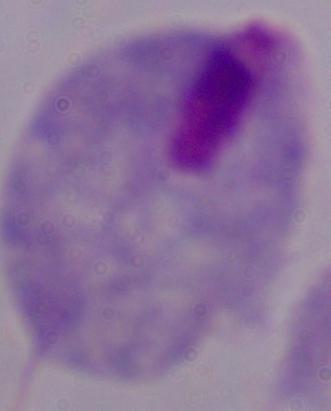
Summary:
  - Magnification: 1000x
  - Identification: trichomonad
  - Modality: micrograph